Assess this cell for malaria.
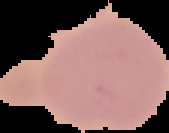

It is uninfected.

{
  "image_type": "cell region segmented out of the field of view; surrounding area masked to black",
  "image_size": "169×133 pixels",
  "preparation": "thin blood film"
}